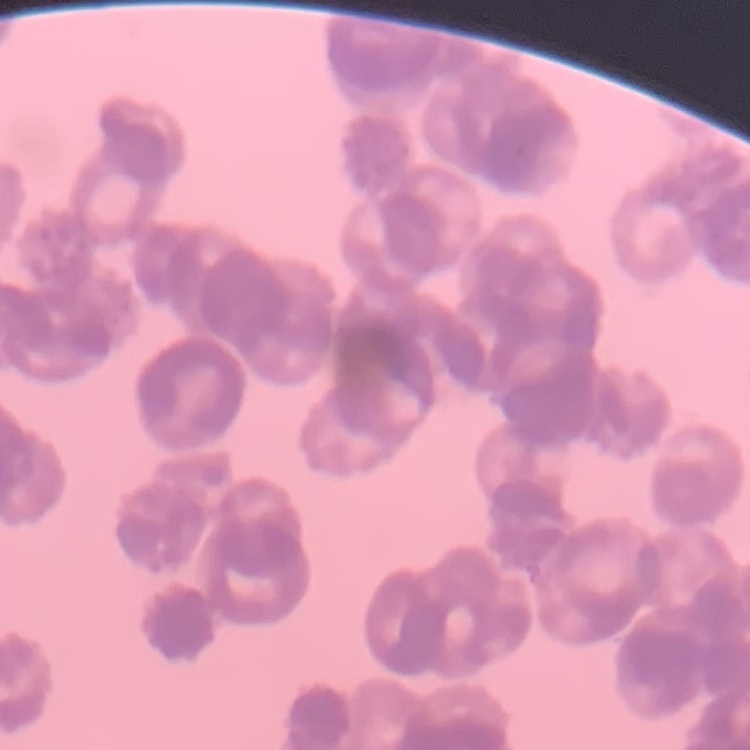
Summary:
  - Red blood cell morphology: rouleaux formation
  - Image type: square crop of a larger photomicrograph
  - Stain: Field's or Giemsa
  - Preparation: thin blood smear